Name the blood parasite species.
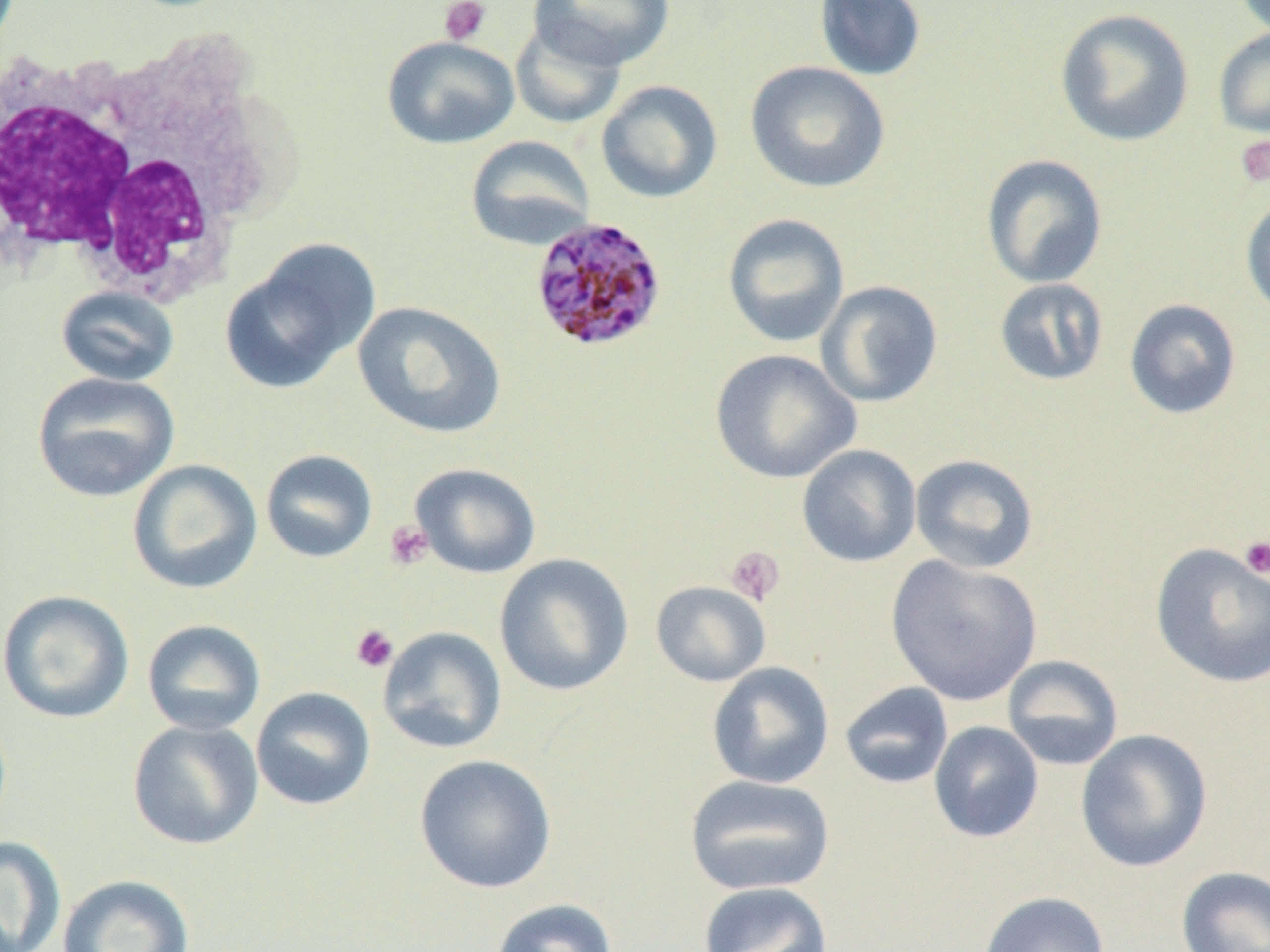
Plasmodium malariae.

Approximate bounding boxes as (x1,y1)-(x2,y2) corner pairs in pixels. Uninfected red blood cell locations: (529,0)-(674,70), (814,0)-(927,82), (1232,0)-(1270,38), (1054,8)-(1194,147), (510,16)-(626,129), (1212,28)-(1270,140), (382,35)-(519,149), (745,60)-(890,193), (596,80)-(723,204), (465,135)-(597,252), (981,153)-(1108,288), (1240,195)-(1270,321), (722,213)-(850,348), (220,242)-(379,394), (993,277)-(1110,387), (815,280)-(943,408), (56,286)-(179,387), (1124,298)-(1242,419), (352,301)-(506,440), (709,348)-(861,484), (32,372)-(180,503), (797,444)-(922,568), (261,448)-(378,563), (909,453)-(1040,574), (128,459)-(263,595), (409,462)-(541,579), (1150,543)-(1270,689), (494,553)-(634,696), (885,555)-(1042,706), (651,580)-(770,687), (1,590)-(134,724), (142,618)-(266,735), (377,626)-(507,754), (1001,655)-(1124,770), (707,662)-(835,789), (839,682)-(953,790), (250,686)-(376,811), (127,718)-(264,850), (928,721)-(1044,843), (1076,728)-(1213,872), (413,754)-(557,893), (684,774)-(835,897), (0,835)-(67,952), (1176,866)-(1270,952), (57,874)-(194,952), (698,881)-(834,952), (978,891)-(1111,952), (489,898)-(618,952). Platelet locations: (439,0)-(491,45), (1234,134)-(1270,189), (384,520)-(433,571), (1239,537)-(1270,580), (725,546)-(785,607), (350,623)-(398,673). Plasmodium malariae-infected red blood cell locations: (529,215)-(667,352). White blood cell locations: (0,31)-(284,312). Light microscopy. Captured at 1000x magnification. One field of a larger specimen. Image is 1270×952 pixels. Thin blood film.